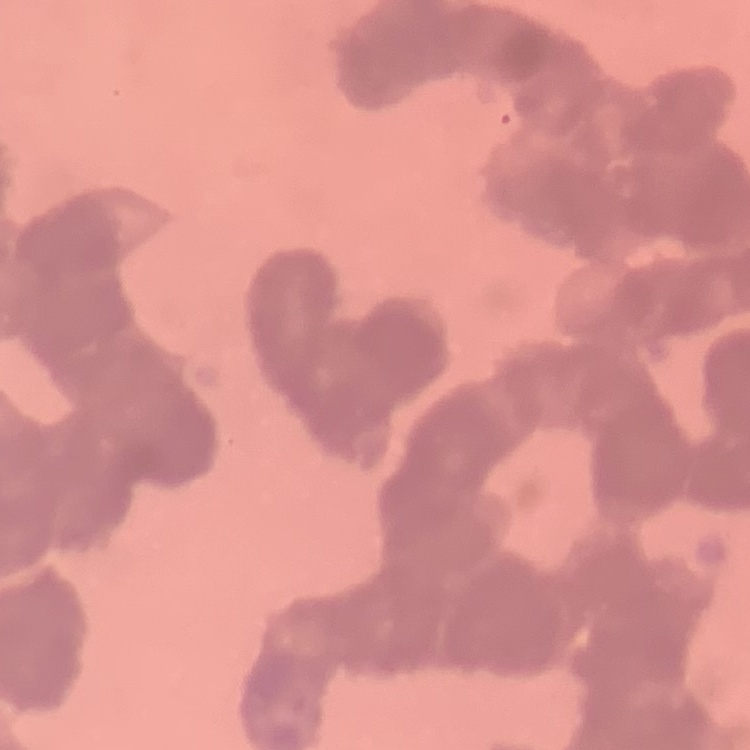

The red blood cells show rouleaux formation. Thin blood film. Stained with either Field's or Giemsa. One tile cut from a larger photomicrograph.